Report the malaria status of this cell.
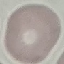
Uninfected.

Giemsa-stained preparation. Acquired by smartphone through the microscope eyepiece. Thin smear of blood. Cell patch, automatically extracted from a larger field of view and resized to 64 × 64 pixels.